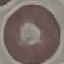
Result: no malaria parasites seen. Giemsa-stained preparation. Cell patch, automatically extracted from a larger field of view and resized to 64 × 64 pixels. Thin blood smear. Acquired by smartphone through the microscope eyepiece.